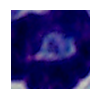
{
  "identification": "white blood cell",
  "modality": "micrograph",
  "magnification": "1000x"
}